Draw a bounding box around every leukocyte (white blood cell).
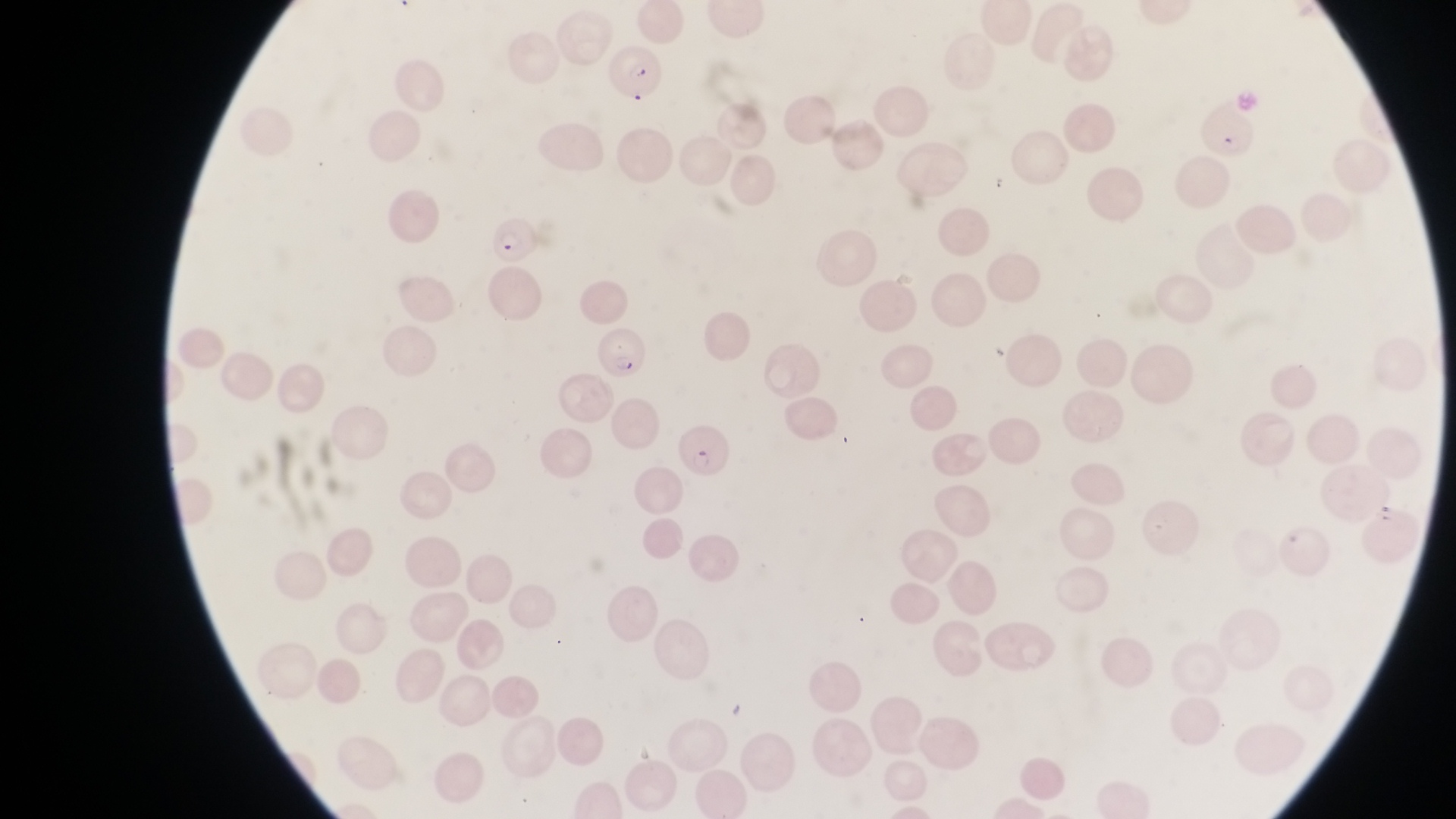
No leukocytes observed.

magnification: 1000x
preparation: thin blood film
field_of_view: single
country: Uganda
capture: smartphone photograph through the eyepiece of an Olympus CX-23 microscope
parasitised_red_blood_cell_locations: 'approximate bounding boxes as left top right bottom in pixels: 602 47 660 94; 1191 96 1255 159; 483 217 539 269; 591 328 651 378; 673 419 731 480'
image_size: 1456×819 pixels